Assess for malaria.
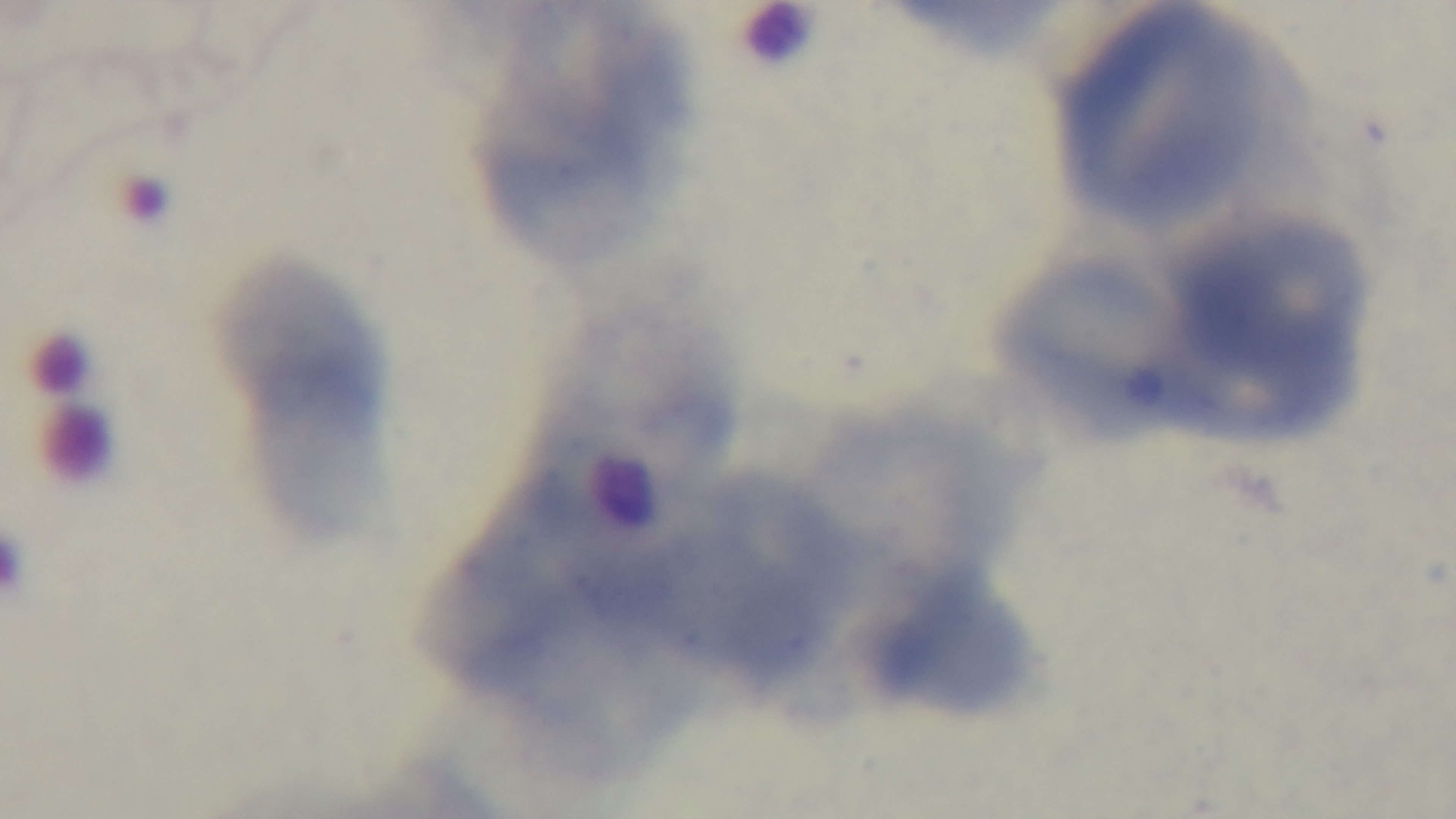
Uninfected.

Summary:
  - Capture: mounted 4K digital camera
  - Modality: light microscopy
  - Objective: 100x oil immersion
  - Stain: Giemsa
  - Preparation: thin smear
  - Field of view: one from the slide